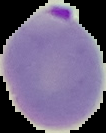

result: malaria parasites detected
image_size: 106×133 pixels
preparation: thin blood film
image_type: cell region segmented out of the field of view; surrounding area masked to black